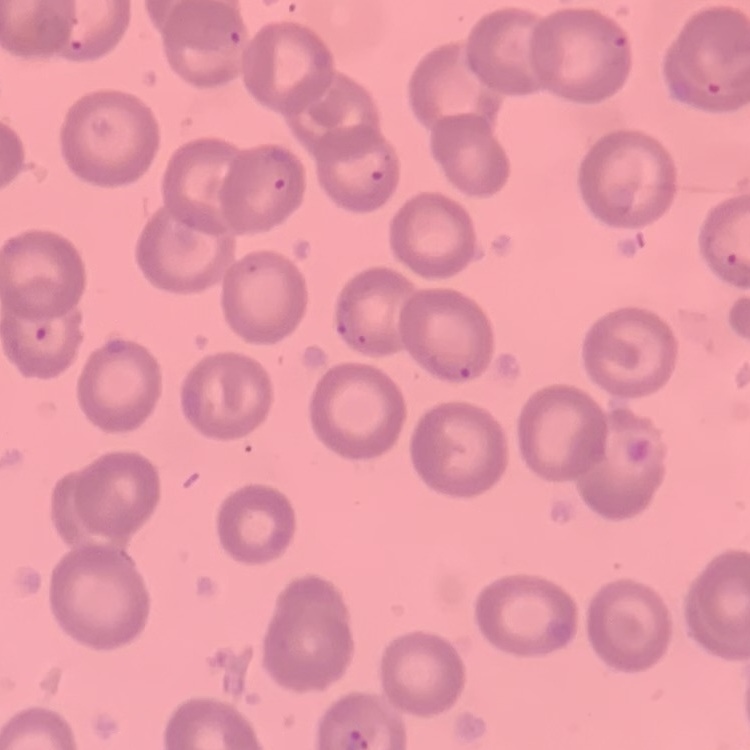

erythrocyte morphology = no rouleaux formation
preparation = thin peripheral smear
image type = square crop of a larger photomicrograph
stain = Field's or Giemsa